Comment on the morphology of the erythrocytes.
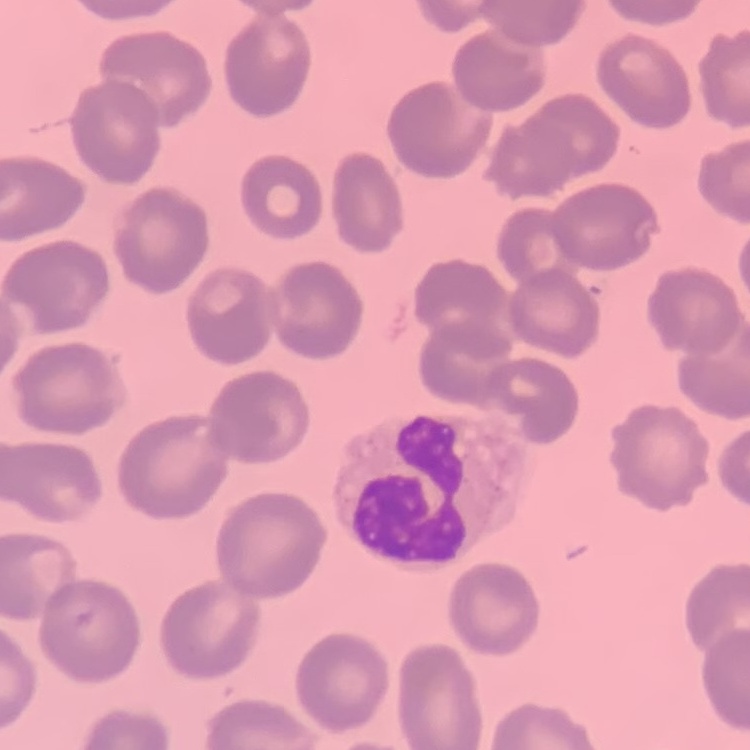
No rouleaux formation.

Summary:
  - Preparation: thin peripheral smear
  - Stain: Field's or Giemsa
  - Image type: one tile cut from a larger photomicrograph